Classify this cell by malaria status.
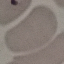

It is uninfected.

Giemsa stain. Acquired by smartphone through the microscope eyepiece. Cell patch, automatically extracted from a larger field of view and resized to 64 × 64 pixels. Thin blood film.